Assess this cell for malaria.
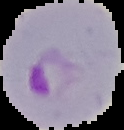
Parasitized.

image type = segmented cell region on a black background
image size = 124×130 pixels
preparation = thin blood smear